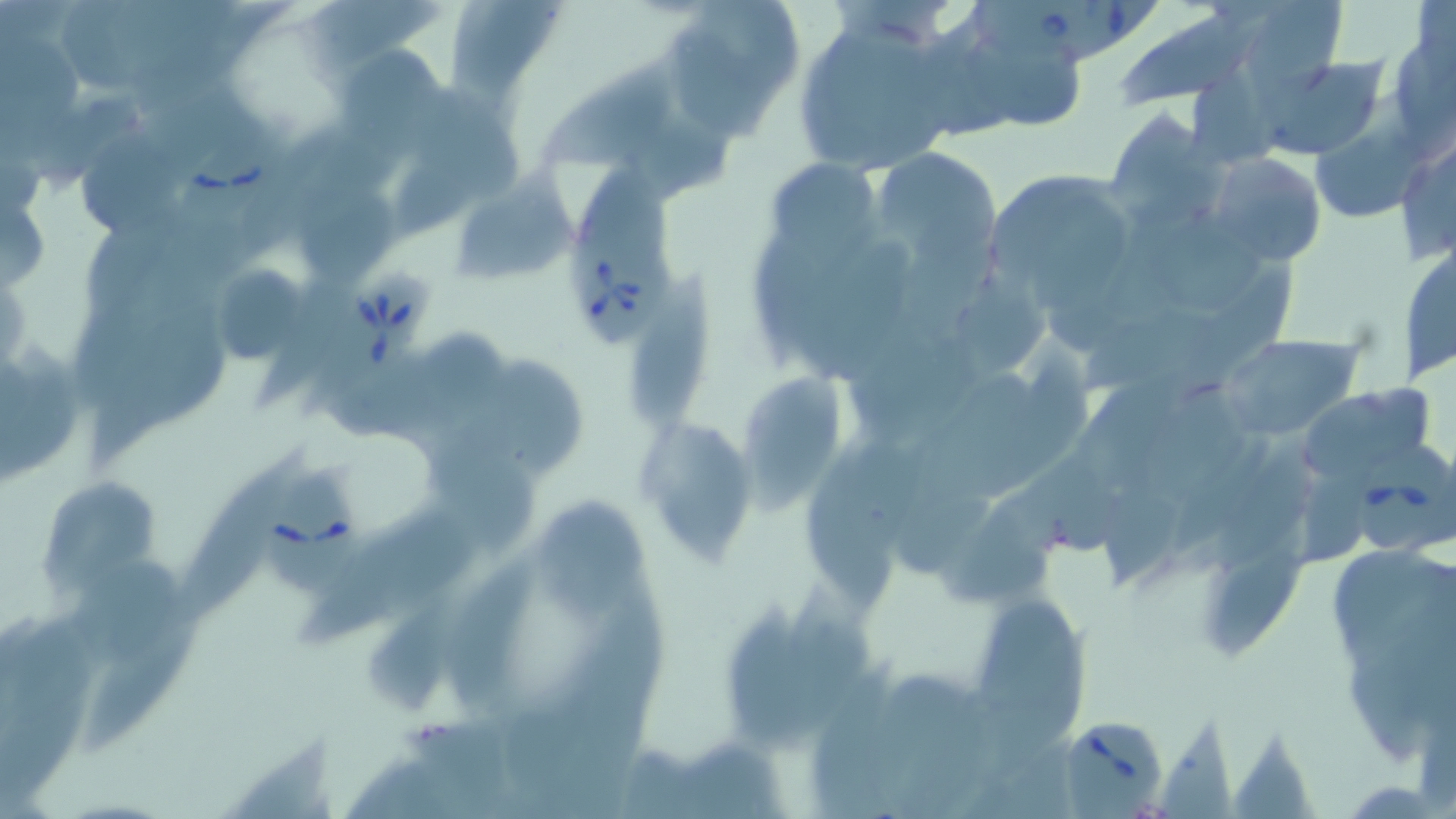 Approximate bounding boxes as (x1,y1)-(x2,y2) corner pairs in pixels. Uninfected red blood cell locations: (59,0)-(140,87), (300,0)-(442,65), (445,0)-(568,100), (659,0)-(806,136), (1244,0)-(1348,87), (1116,10)-(1272,106), (790,16)-(970,175), (963,32)-(1086,128), (2,34)-(82,136), (1399,42)-(1456,151), (333,45)-(444,147), (1245,50)-(1395,162), (542,57)-(676,165), (1194,68)-(1276,165), (151,87)-(261,167), (1304,87)-(1437,219), (27,88)-(147,198), (413,88)-(528,195), (631,109)-(742,208), (1102,109)-(1223,234), (76,132)-(190,237), (1394,134)-(1456,266), (872,148)-(1000,274), (1204,154)-(1327,269), (764,158)-(882,260), (579,159)-(667,252), (984,168)-(1144,308), (453,172)-(579,287), (298,183)-(400,280), (1,205)-(45,294), (87,216)-(177,316), (745,224)-(832,364), (1147,226)-(1269,312), (1398,236)-(1455,386), (1190,252)-(1299,388), (629,261)-(716,426), (206,263)-(313,366), (957,273)-(1052,371), (1085,301)-(1225,391), (90,321)-(225,467), (845,327)-(947,445), (425,332)-(512,414), (1215,334)-(1363,440), (4,339)-(82,471), (1004,340)-(1096,485), (494,358)-(587,473), (738,373)-(848,506), (1297,384)-(1439,486), (1149,389)-(1253,504), (636,420)-(760,564), (432,436)-(535,555), (178,447)-(308,625), (1221,447)-(1314,566), (1026,462)-(1129,553), (1303,464)-(1377,562), (804,467)-(894,610), (37,477)-(162,593), (890,487)-(1000,576), (1106,491)-(1182,589), (535,493)-(646,610), (304,503)-(477,646), (945,509)-(1061,606), (1208,546)-(1310,657), (1334,550)-(1452,658), (441,557)-(537,707), (71,558)-(184,658), (783,581)-(870,730), (576,586)-(666,728), (726,601)-(804,742), (977,601)-(1080,713), (80,607)-(201,760), (370,609)-(450,710), (1349,647)-(1435,767), (807,653)-(901,819), (508,687)-(582,799), (1161,712)-(1235,819), (400,720)-(516,807), (223,728)-(340,819), (1235,728)-(1321,819), (995,729)-(1086,819), (691,736)-(790,819), (617,741)-(708,819). Babesia divergens-infected red blood cell locations: (968,0)-(1089,64), (1061,0)-(1163,63), (182,133)-(292,218), (572,238)-(672,350), (311,274)-(433,419), (1349,439)-(1453,553), (262,470)-(365,592), (1058,716)-(1169,818). Slide-level diagnosis: Babesia divergens. Optical microscopy. Thin blood smear. One field of a larger specimen. Image is 1456×819 pixels. 1000x magnification. May-Grünwald-Giemsa stain.